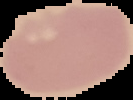
result = no malaria parasites seen
image type = segmented cell region with the area outside set to black
preparation = thin blood film
image size = 133×100 pixels